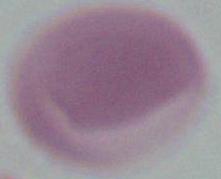

An erythrocyte is shown. 1000x magnification. Photomicrograph.